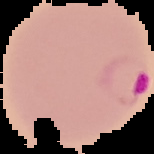

malaria status = parasitized
preparation = thin blood smear
image type = segmented cell region on a black background
image size = 154×154 pixels